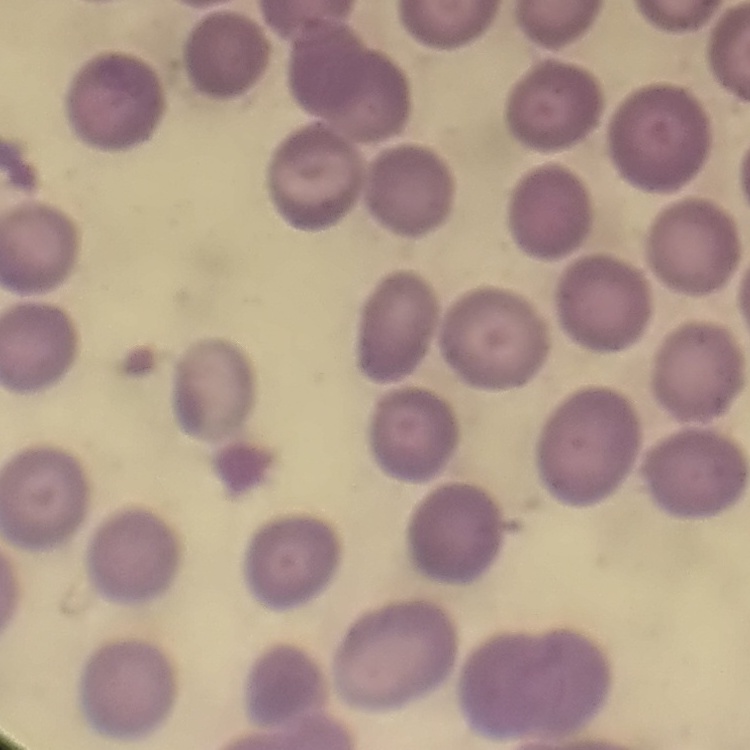
Summary:
  - Red blood cell morphology: no rouleaux formation
  - Stain: Field's or Giemsa
  - Preparation: thin blood film
  - Image type: one tile cut from a larger photomicrograph